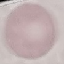
Summary:
  - Result: negative for malaria parasites
  - Capture: smartphone through the microscope eyepiece
  - Image type: cell patch, automatically extracted from a larger field of view and resized to 64 × 64 pixels
  - Preparation: thin smear
  - Stain: Giemsa